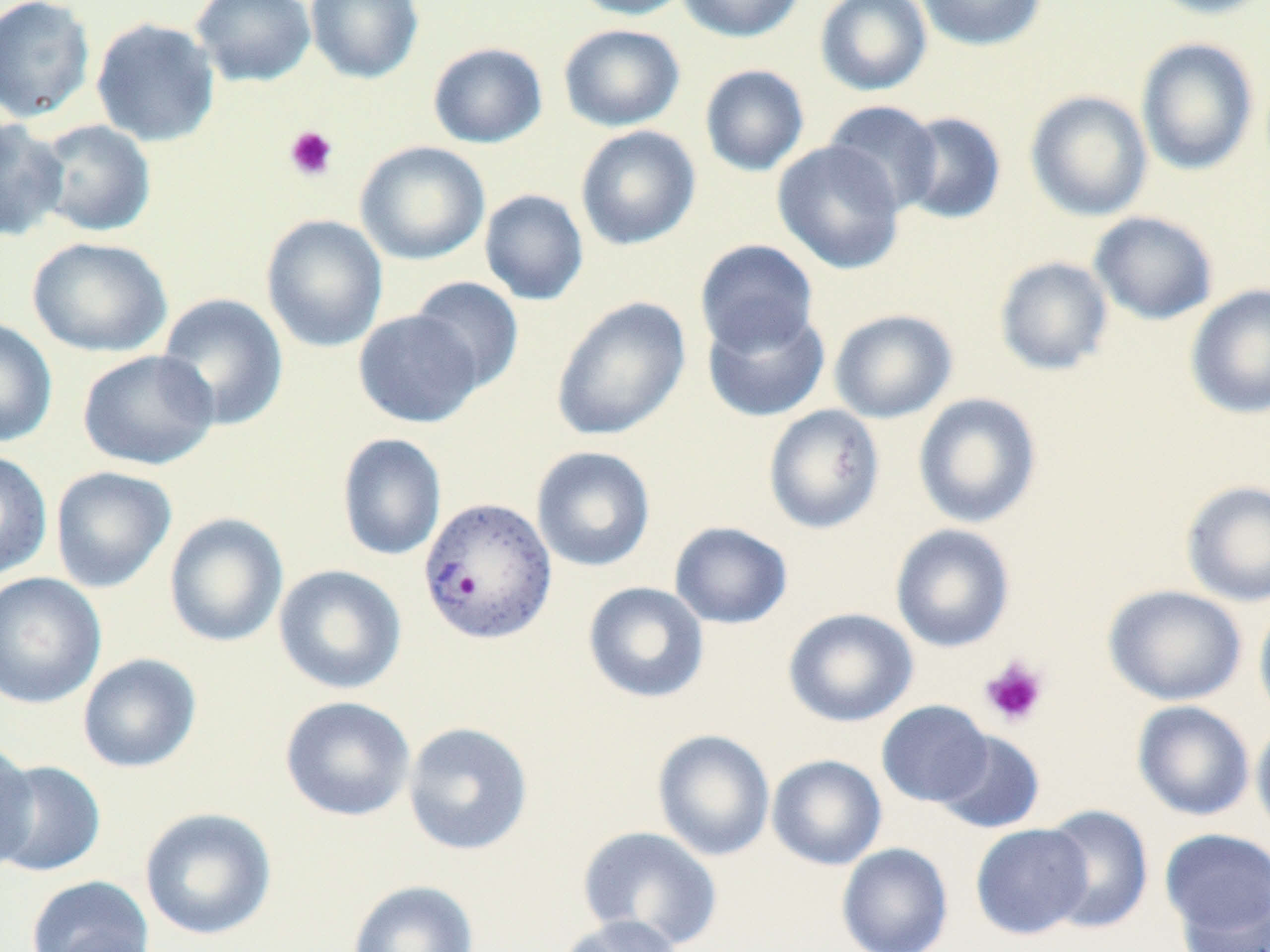

{
  "slide_level_diagnosis": "Plasmodium vivax",
  "platelet_locations": "approximate bounding boxes as [x1, y1, x2, y2] in pixels: [284, 125, 338, 181], [980, 656, 1049, 728]",
  "modality": "optical microscopy",
  "preparation": "thin blood film",
  "plasmodium_vivax_infected_red_blood_cell_locations": "approximate bounding boxes as [x1, y1, x2, y2] in pixels: [417, 495, 557, 646]",
  "field_of_view": "one of a larger specimen",
  "uninfected_red_blood_cell_locations": "approximate bounding boxes as [x1, y1, x2, y2] in pixels: [0, 0, 95, 123], [189, 0, 317, 87], [304, 0, 424, 83], [568, 0, 694, 20], [676, 0, 805, 43], [815, 0, 932, 96], [915, 0, 1047, 51], [1141, 0, 1270, 20], [90, 17, 221, 147], [558, 23, 685, 132], [1135, 37, 1259, 175], [427, 42, 548, 148], [699, 64, 809, 176], [1025, 90, 1153, 221], [822, 100, 943, 216], [898, 111, 1007, 225], [0, 118, 69, 242], [35, 119, 156, 237], [575, 125, 701, 251], [354, 140, 490, 265], [772, 141, 906, 275], [479, 189, 589, 306], [1089, 211, 1219, 325], [261, 214, 389, 353], [27, 237, 172, 357], [695, 239, 819, 356], [994, 256, 1114, 376], [408, 276, 525, 394], [1186, 283, 1270, 420], [156, 293, 289, 431], [551, 296, 691, 441], [701, 305, 831, 423], [352, 309, 483, 428], [829, 309, 958, 424], [0, 315, 58, 448], [78, 349, 219, 470], [913, 392, 1043, 529], [763, 405, 885, 534], [337, 432, 447, 561], [530, 446, 656, 572], [0, 449, 53, 581], [50, 465, 177, 593], [1180, 479, 1270, 606], [164, 512, 289, 648], [669, 521, 793, 629], [890, 524, 1016, 653], [273, 564, 407, 695], [0, 571, 106, 709], [583, 581, 710, 704], [1103, 584, 1248, 706], [1253, 598, 1270, 728], [783, 607, 919, 727], [77, 653, 202, 773], [279, 695, 416, 822], [876, 700, 993, 807], [1132, 700, 1255, 821], [1251, 715, 1270, 841], [402, 721, 534, 856], [652, 729, 775, 861], [933, 730, 1045, 834], [0, 736, 38, 871], [767, 754, 887, 870], [0, 760, 106, 878], [1040, 804, 1154, 934], [139, 806, 277, 941], [970, 823, 1093, 939], [576, 825, 723, 950], [1159, 828, 1270, 945], [836, 842, 953, 952], [26, 875, 155, 952], [347, 879, 479, 952], [1177, 890, 1270, 952], [553, 915, 687, 952]",
  "magnification": "1000x",
  "stain": "May-Grünwald-Giemsa",
  "image_size": "1270×952 pixels"
}